Report the malaria status of this cell.
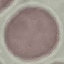
It is uninfected.

Acquired by smartphone through the microscope eyepiece. Giemsa stain. Cell patch, automatically extracted from a larger field of view and resized to 64 × 64 pixels. Thin blood smear.